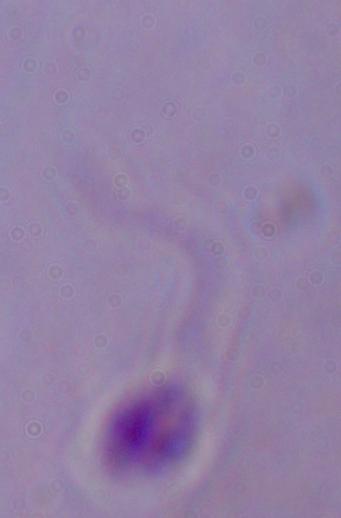

modality = micrograph
identification = Leishmania
magnification = 1000x